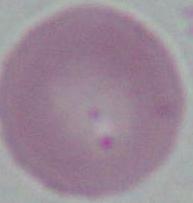

{
  "modality": "photomicrograph",
  "identification": "erythrocyte",
  "magnification": "1000x"
}